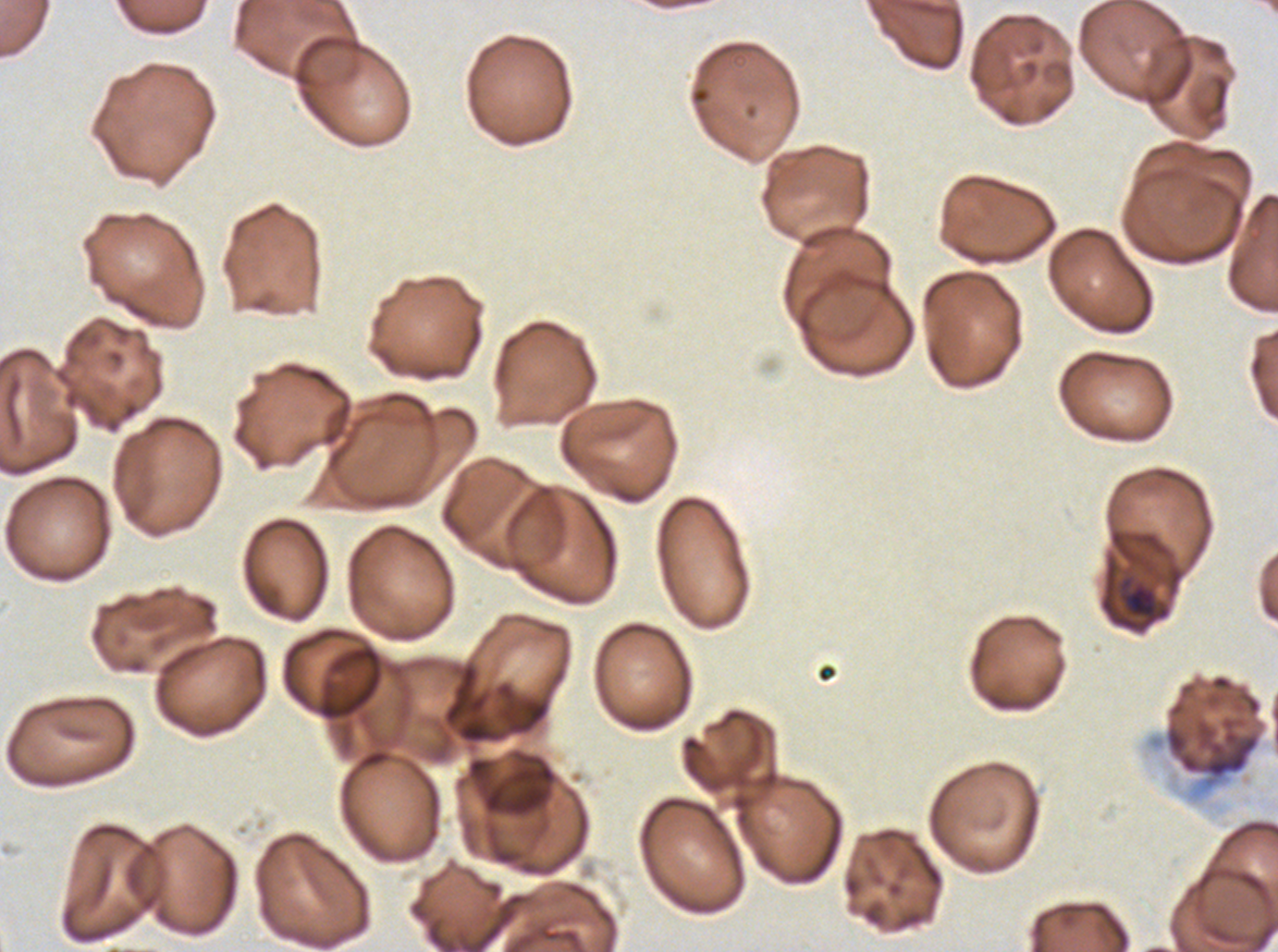
Approximate bounding boxes as (x1, y1, x2, y2) in pixels.
Summary:
  - Late-ring/early-trophozoite locations: (1120, 581, 1170, 629)
  - Specimen: P. falciparum cultured ex vivo for 24 to 48 hours, from a patient in The Gambia
  - Stain: Giemsa
  - Image size: 1278×952 pixels
  - Field of view: sub-image separated from a larger composite
  - Preparation: thin blood film